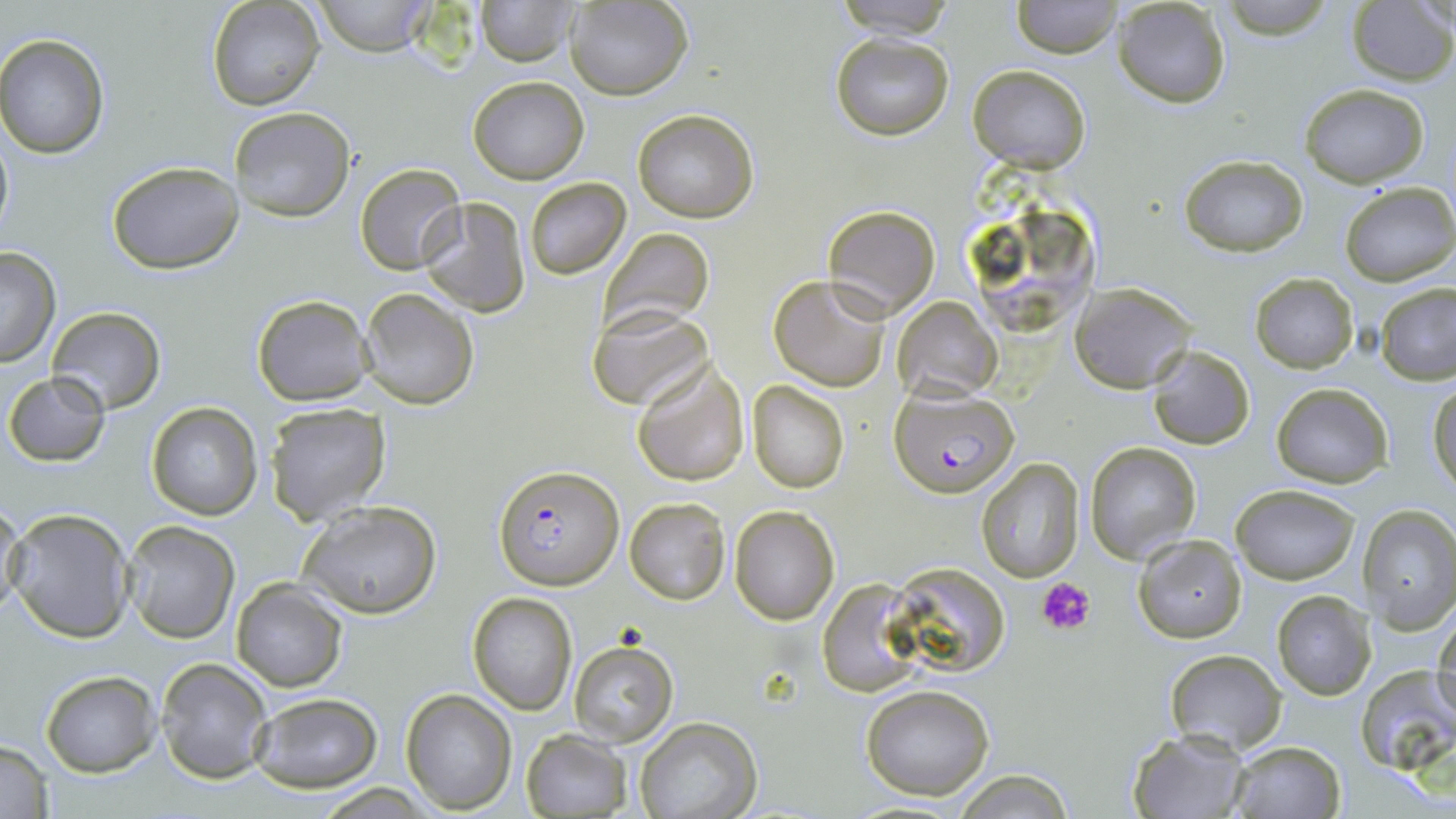
Summary:
  - Coordinate format: approximate bounding boxes as named x1/y1/x2/y2 corners in pixels
  - Plasmodium falciparum-infected red blood cell locations: (x1=891, y1=390, x2=1019, y2=497), (x1=496, y1=464, x2=623, y2=590)
  - Platelet locations: (x1=1037, y1=576, x2=1097, y2=635)
  - Uninfected red blood cell locations: (x1=204, y1=0, x2=325, y2=111), (x1=315, y1=0, x2=434, y2=56), (x1=473, y1=0, x2=579, y2=68), (x1=565, y1=0, x2=693, y2=100), (x1=832, y1=0, x2=960, y2=38), (x1=1011, y1=0, x2=1122, y2=58), (x1=1113, y1=0, x2=1232, y2=108), (x1=1221, y1=0, x2=1336, y2=38), (x1=1347, y1=2, x2=1456, y2=84), (x1=0, y1=33, x2=110, y2=159), (x1=830, y1=33, x2=954, y2=140), (x1=968, y1=64, x2=1090, y2=172), (x1=467, y1=76, x2=590, y2=184), (x1=1301, y1=83, x2=1429, y2=187), (x1=228, y1=107, x2=356, y2=225), (x1=632, y1=108, x2=760, y2=223), (x1=0, y1=123, x2=14, y2=246), (x1=1178, y1=154, x2=1309, y2=255), (x1=106, y1=161, x2=245, y2=274), (x1=355, y1=163, x2=466, y2=274), (x1=524, y1=178, x2=630, y2=280), (x1=1340, y1=181, x2=1456, y2=288), (x1=417, y1=197, x2=531, y2=317), (x1=823, y1=204, x2=940, y2=319), (x1=598, y1=227, x2=715, y2=333), (x1=0, y1=249, x2=61, y2=367), (x1=1249, y1=272, x2=1359, y2=373), (x1=769, y1=274, x2=890, y2=390), (x1=1070, y1=282, x2=1199, y2=392), (x1=1375, y1=284, x2=1456, y2=385), (x1=358, y1=287, x2=479, y2=411), (x1=251, y1=293, x2=375, y2=407), (x1=893, y1=296, x2=1003, y2=403), (x1=46, y1=306, x2=165, y2=415), (x1=590, y1=308, x2=714, y2=412), (x1=1148, y1=345, x2=1254, y2=449), (x1=631, y1=361, x2=751, y2=487), (x1=4, y1=372, x2=110, y2=466), (x1=747, y1=382, x2=849, y2=493), (x1=1429, y1=382, x2=1456, y2=493), (x1=1272, y1=383, x2=1393, y2=488), (x1=146, y1=401, x2=262, y2=520), (x1=263, y1=402, x2=391, y2=525), (x1=1083, y1=442, x2=1201, y2=564), (x1=974, y1=458, x2=1085, y2=583), (x1=1230, y1=484, x2=1360, y2=585), (x1=625, y1=498, x2=730, y2=604), (x1=298, y1=499, x2=443, y2=619), (x1=1, y1=500, x2=26, y2=619), (x1=730, y1=504, x2=841, y2=624), (x1=1358, y1=506, x2=1456, y2=633), (x1=5, y1=509, x2=134, y2=643), (x1=120, y1=521, x2=239, y2=644), (x1=1132, y1=535, x2=1248, y2=643), (x1=886, y1=564, x2=1012, y2=677), (x1=230, y1=578, x2=348, y2=692), (x1=815, y1=580, x2=927, y2=698), (x1=1271, y1=590, x2=1377, y2=701), (x1=466, y1=593, x2=576, y2=715), (x1=1434, y1=615, x2=1456, y2=725), (x1=569, y1=641, x2=678, y2=745), (x1=1163, y1=649, x2=1288, y2=755), (x1=155, y1=659, x2=272, y2=785), (x1=1355, y1=665, x2=1455, y2=776), (x1=41, y1=671, x2=161, y2=776), (x1=860, y1=683, x2=994, y2=801), (x1=401, y1=688, x2=517, y2=814), (x1=248, y1=691, x2=384, y2=793), (x1=636, y1=717, x2=762, y2=819), (x1=1127, y1=730, x2=1246, y2=818), (x1=522, y1=731, x2=630, y2=818), (x1=0, y1=739, x2=55, y2=818), (x1=1233, y1=741, x2=1343, y2=818), (x1=951, y1=768, x2=1074, y2=819)
  - Slide-level diagnosis: Plasmodium falciparum
  - Field of view: one of a larger specimen
  - Image size: 1456×819 pixels
  - Magnification: 1000x
  - Preparation: thin blood smear
  - Modality: optical microscopy
  - Stain: May-Grünwald-Giemsa